Outline each Trypanosoma brucei.
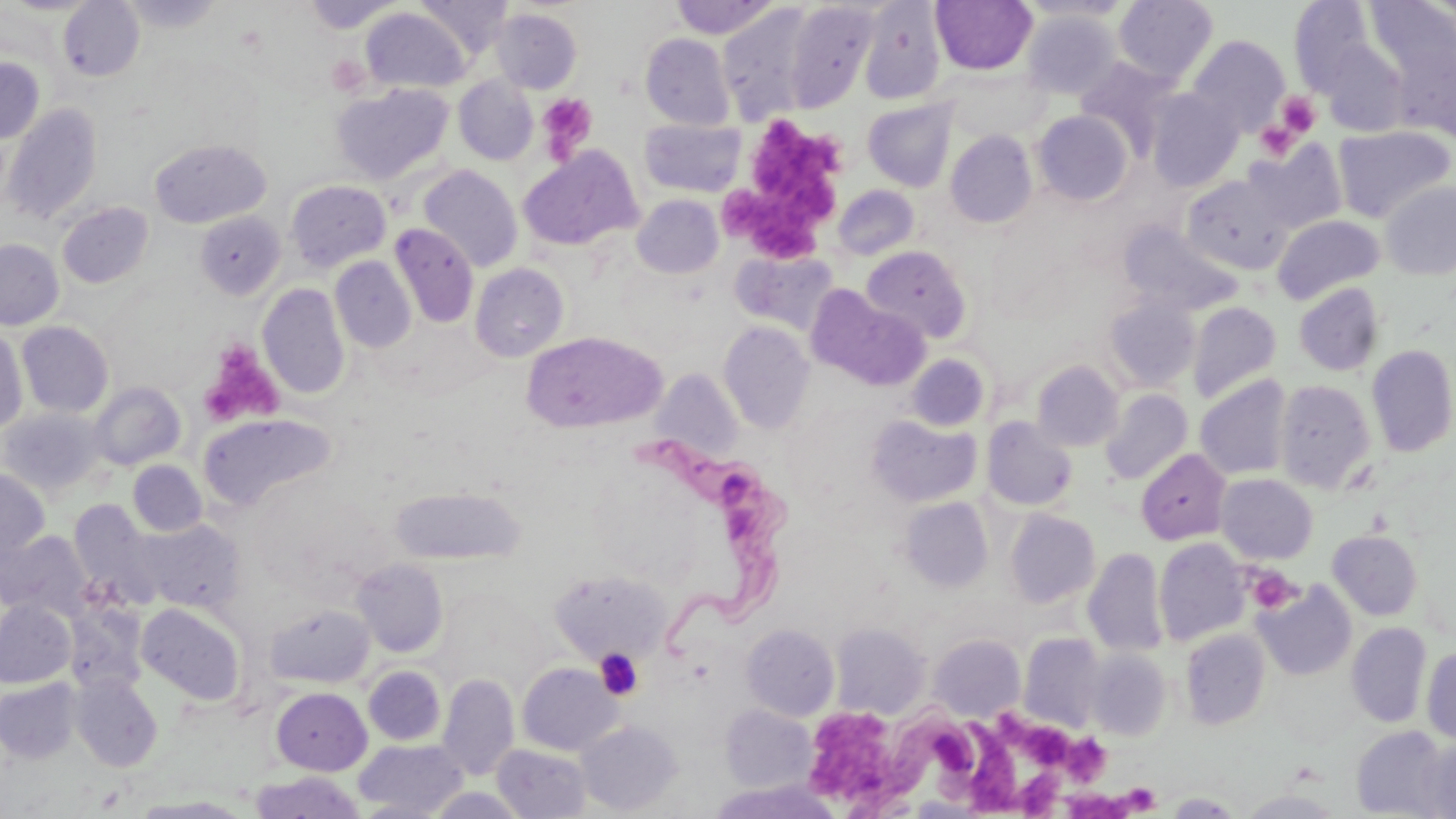
Approximate bounding boxes as named x1/y1/x2/y2 corners in pixels.
Trypanosoma brucei: (x1=626, y1=431, x2=790, y2=651), (x1=846, y1=710, x2=980, y2=817).

Platelet locations: (x1=326, y1=56, x2=369, y2=96), (x1=1276, y1=92, x2=1322, y2=136), (x1=537, y1=93, x2=597, y2=160), (x1=753, y1=117, x2=847, y2=215), (x1=1255, y1=121, x2=1298, y2=161), (x1=725, y1=191, x2=776, y2=241), (x1=756, y1=214, x2=820, y2=257), (x1=200, y1=341, x2=282, y2=427), (x1=1245, y1=566, x2=1300, y2=614), (x1=594, y1=648, x2=644, y2=700), (x1=993, y1=712, x2=1034, y2=750), (x1=814, y1=715, x2=889, y2=793), (x1=963, y1=721, x2=1022, y2=817), (x1=1026, y1=723, x2=1070, y2=776), (x1=1063, y1=733, x2=1110, y2=785), (x1=1016, y1=764, x2=1062, y2=819), (x1=1119, y1=783, x2=1161, y2=814), (x1=1061, y1=789, x2=1134, y2=818). Uninfected red blood cell locations: (x1=58, y1=0, x2=145, y2=82), (x1=120, y1=0, x2=225, y2=33), (x1=415, y1=0, x2=513, y2=56), (x1=669, y1=0, x2=782, y2=39), (x1=931, y1=0, x2=1037, y2=75), (x1=1018, y1=0, x2=1135, y2=22), (x1=1113, y1=0, x2=1218, y2=84), (x1=302, y1=1, x2=403, y2=32), (x1=1289, y1=1, x2=1374, y2=95), (x1=784, y1=2, x2=877, y2=111), (x1=859, y1=2, x2=946, y2=105), (x1=1365, y1=2, x2=1456, y2=84), (x1=717, y1=6, x2=817, y2=121), (x1=360, y1=7, x2=471, y2=93), (x1=492, y1=8, x2=582, y2=93), (x1=1021, y1=10, x2=1121, y2=99), (x1=640, y1=33, x2=735, y2=129), (x1=1187, y1=34, x2=1290, y2=136), (x1=1321, y1=41, x2=1409, y2=136), (x1=1405, y1=44, x2=1456, y2=145), (x1=0, y1=57, x2=44, y2=144), (x1=1075, y1=57, x2=1179, y2=155), (x1=943, y1=67, x2=1049, y2=141), (x1=454, y1=76, x2=538, y2=165), (x1=332, y1=83, x2=453, y2=185), (x1=1147, y1=89, x2=1243, y2=191), (x1=863, y1=99, x2=958, y2=192), (x1=3, y1=103, x2=102, y2=225), (x1=1033, y1=111, x2=1133, y2=206), (x1=640, y1=119, x2=746, y2=197), (x1=1333, y1=125, x2=1454, y2=223), (x1=945, y1=130, x2=1038, y2=229), (x1=150, y1=139, x2=270, y2=228), (x1=1245, y1=142, x2=1347, y2=235), (x1=519, y1=149, x2=641, y2=251), (x1=418, y1=165, x2=523, y2=272), (x1=1182, y1=175, x2=1291, y2=274), (x1=285, y1=180, x2=391, y2=272), (x1=1380, y1=182, x2=1456, y2=280), (x1=833, y1=185, x2=920, y2=261), (x1=632, y1=194, x2=723, y2=278), (x1=57, y1=202, x2=153, y2=289), (x1=194, y1=211, x2=286, y2=300), (x1=1273, y1=215, x2=1385, y2=305), (x1=1118, y1=221, x2=1242, y2=316), (x1=389, y1=223, x2=479, y2=328), (x1=0, y1=239, x2=63, y2=330), (x1=860, y1=245, x2=972, y2=343), (x1=731, y1=249, x2=841, y2=336), (x1=330, y1=257, x2=416, y2=353), (x1=470, y1=263, x2=569, y2=362), (x1=258, y1=283, x2=350, y2=399), (x1=1293, y1=284, x2=1384, y2=376), (x1=808, y1=288, x2=930, y2=391), (x1=1104, y1=297, x2=1200, y2=391), (x1=1187, y1=301, x2=1282, y2=404), (x1=17, y1=321, x2=114, y2=417), (x1=719, y1=321, x2=815, y2=434), (x1=0, y1=326, x2=28, y2=435), (x1=521, y1=331, x2=666, y2=434), (x1=1367, y1=344, x2=1456, y2=458), (x1=905, y1=353, x2=989, y2=432), (x1=1032, y1=360, x2=1123, y2=451), (x1=651, y1=370, x2=743, y2=460), (x1=1195, y1=375, x2=1292, y2=480), (x1=1275, y1=379, x2=1375, y2=495), (x1=88, y1=381, x2=186, y2=470), (x1=1100, y1=389, x2=1193, y2=485), (x1=0, y1=408, x2=107, y2=498), (x1=199, y1=412, x2=338, y2=511), (x1=866, y1=415, x2=981, y2=507), (x1=982, y1=417, x2=1077, y2=511), (x1=1136, y1=448, x2=1231, y2=545), (x1=128, y1=461, x2=207, y2=536), (x1=591, y1=467, x2=705, y2=586), (x1=0, y1=468, x2=49, y2=564), (x1=1216, y1=474, x2=1318, y2=564), (x1=390, y1=486, x2=523, y2=564), (x1=900, y1=497, x2=993, y2=592), (x1=70, y1=500, x2=164, y2=611), (x1=1004, y1=509, x2=1099, y2=608), (x1=137, y1=519, x2=244, y2=614), (x1=0, y1=530, x2=93, y2=622), (x1=1328, y1=530, x2=1423, y2=620), (x1=1154, y1=538, x2=1250, y2=647), (x1=1084, y1=547, x2=1168, y2=657), (x1=351, y1=559, x2=448, y2=657), (x1=549, y1=570, x2=671, y2=664), (x1=1254, y1=582, x2=1356, y2=681), (x1=0, y1=600, x2=76, y2=688), (x1=64, y1=603, x2=148, y2=695), (x1=136, y1=603, x2=247, y2=705), (x1=266, y1=604, x2=375, y2=688), (x1=1346, y1=622, x2=1432, y2=727), (x1=831, y1=623, x2=930, y2=718), (x1=741, y1=624, x2=839, y2=720), (x1=1181, y1=629, x2=1270, y2=731), (x1=1019, y1=633, x2=1106, y2=732), (x1=929, y1=634, x2=1025, y2=721), (x1=1421, y1=646, x2=1456, y2=743), (x1=1086, y1=650, x2=1171, y2=741), (x1=517, y1=662, x2=621, y2=755), (x1=364, y1=666, x2=445, y2=745), (x1=438, y1=673, x2=519, y2=781), (x1=70, y1=674, x2=163, y2=771), (x1=0, y1=678, x2=81, y2=763), (x1=271, y1=687, x2=372, y2=775), (x1=720, y1=704, x2=815, y2=792), (x1=577, y1=720, x2=682, y2=815), (x1=1351, y1=726, x2=1451, y2=816), (x1=1421, y1=736, x2=1455, y2=819), (x1=354, y1=738, x2=469, y2=817), (x1=493, y1=743, x2=592, y2=818), (x1=250, y1=771, x2=365, y2=819), (x1=709, y1=780, x2=841, y2=819), (x1=427, y1=788, x2=529, y2=818), (x1=1238, y1=790, x2=1344, y2=818), (x1=1164, y1=792, x2=1244, y2=817), (x1=135, y1=796, x2=251, y2=818). Slide-level diagnosis: Trypanosoma brucei. Single field of view. Thin blood film. 1000x magnification. Image is 1456×819 pixels. Light microscopy. May-Grünwald-Giemsa stain.